State the blood parasite species.
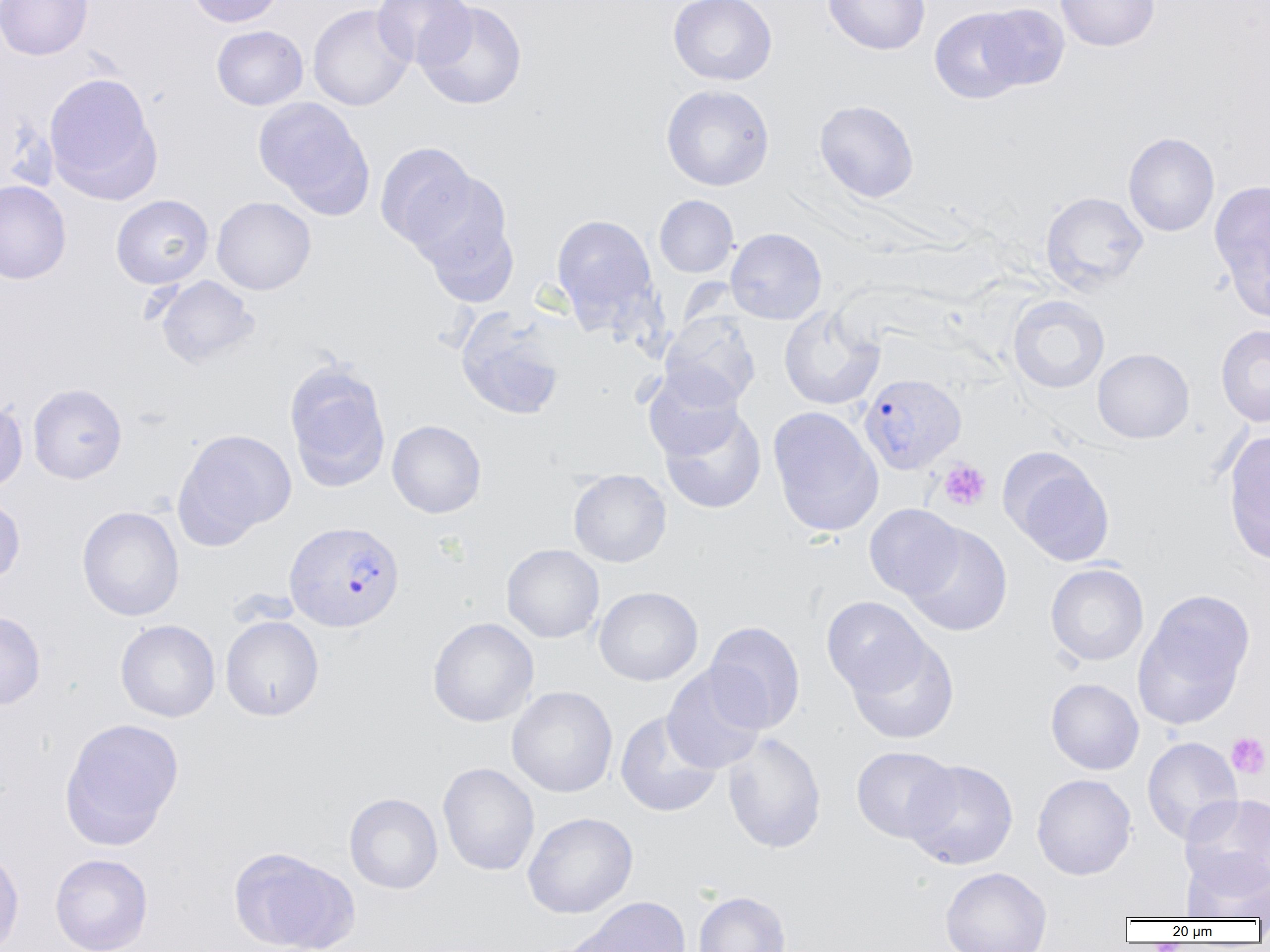
Plasmodium vivax.

Approximate bounding boxes as (x1, y1, x2, y2) in pixels. Plasmodium vivax-infected red blood cell locations: (862, 378, 970, 479), (284, 521, 405, 632). Uninfected red blood cell locations: (1, 0, 93, 60), (186, 0, 285, 27), (372, 0, 475, 70), (668, 0, 778, 85), (823, 0, 930, 55), (1056, 0, 1160, 51), (415, 1, 528, 109), (977, 3, 1069, 91), (308, 4, 414, 111), (930, 7, 1029, 103), (211, 25, 308, 110), (44, 72, 161, 201), (660, 84, 774, 191), (253, 98, 373, 216), (814, 99, 919, 203), (1123, 132, 1219, 236), (375, 142, 478, 251), (408, 170, 520, 304), (1209, 179, 1270, 318), (0, 181, 71, 284), (1040, 191, 1148, 294), (111, 194, 214, 289), (654, 195, 738, 278), (211, 196, 316, 295), (551, 213, 658, 326), (726, 227, 827, 324), (153, 275, 259, 369), (1007, 296, 1110, 394), (779, 305, 884, 410), (454, 307, 569, 420), (661, 311, 761, 409), (1216, 324, 1270, 427), (1092, 348, 1194, 444), (284, 361, 391, 491), (642, 368, 744, 461), (28, 383, 127, 484), (0, 398, 28, 495), (659, 406, 767, 514), (768, 410, 883, 541), (387, 420, 487, 518), (174, 428, 296, 546), (1223, 430, 1270, 564), (1001, 449, 1116, 566), (568, 469, 671, 567), (0, 493, 25, 587), (864, 504, 965, 600), (77, 506, 185, 621), (904, 524, 1013, 637), (502, 543, 604, 643), (1045, 563, 1149, 666), (593, 586, 703, 686), (1134, 590, 1254, 729), (822, 596, 929, 696), (0, 611, 46, 711), (220, 615, 324, 721), (427, 617, 539, 727), (115, 619, 220, 722), (703, 620, 805, 734), (846, 634, 960, 745), (662, 665, 768, 774), (1045, 678, 1144, 775), (506, 686, 618, 798), (615, 712, 723, 817), (59, 717, 184, 849), (722, 733, 826, 853), (1142, 736, 1243, 844), (851, 745, 959, 843), (903, 759, 1019, 870), (437, 763, 540, 875), (1031, 773, 1137, 880), (344, 792, 443, 894), (1180, 794, 1270, 892), (522, 812, 638, 918), (228, 846, 358, 952), (0, 847, 24, 952), (50, 853, 153, 952), (1182, 854, 1270, 922), (940, 867, 1052, 952), (692, 890, 792, 952), (577, 896, 692, 952). Platelet locations: (938, 459, 991, 512), (1226, 733, 1269, 778). Captured at 1000x magnification. Thin blood film. Image is 1270×952 pixels. Optical microscopy. One field of a larger specimen.